Describe the morphology of the erythrocytes.
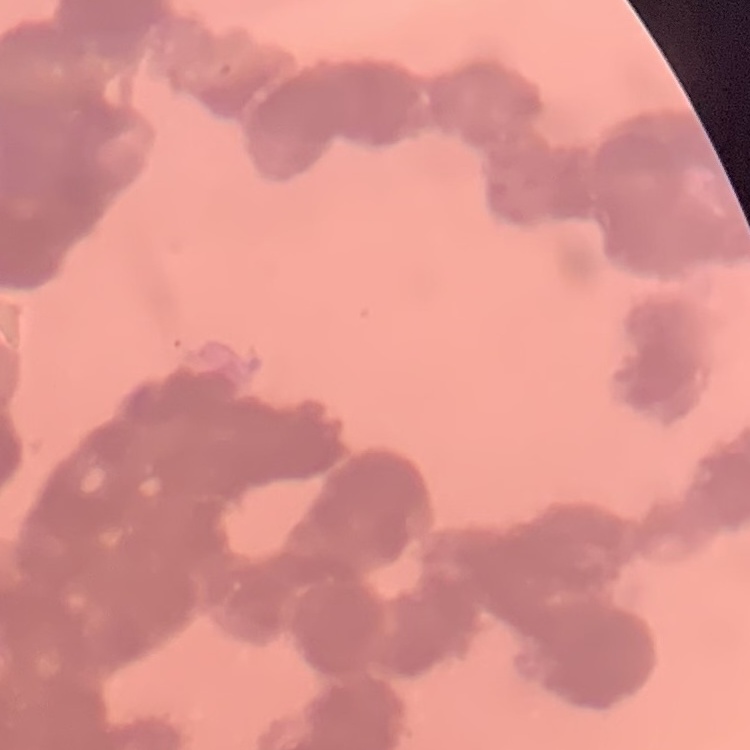
Rouleaux formation.

image_type: one tile cut from a larger photomicrograph
stain: Field's or Giemsa
preparation: thin peripheral smear